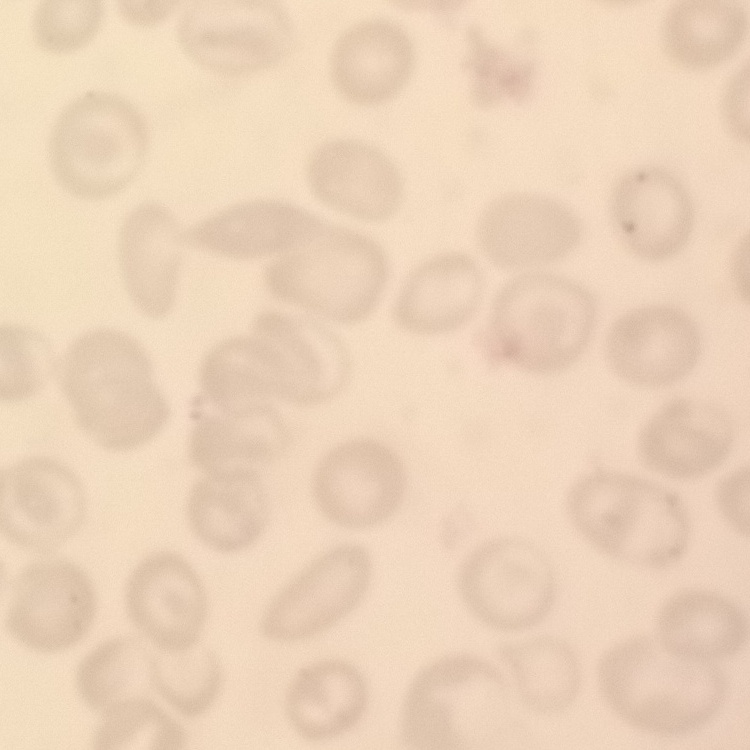
{
  "erythrocyte_morphology": "no rouleaux formation",
  "stain": "Field's or Giemsa",
  "preparation": "thin peripheral smear",
  "image_type": "one tile cut from a larger photomicrograph"
}